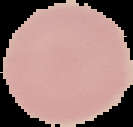

result: no Plasmodium parasites detected
image_type: segmented cell region on a black background
preparation: thin blood smear
image_size: 133×127 pixels